Identify the parasite.
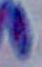

This is Toxoplasma gondii.

Summary:
  - Modality: micrograph
  - Magnification: 1000x